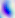

Summary:
  - Identification: Toxoplasma gondii
  - Magnification: 400x
  - Modality: photomicrograph